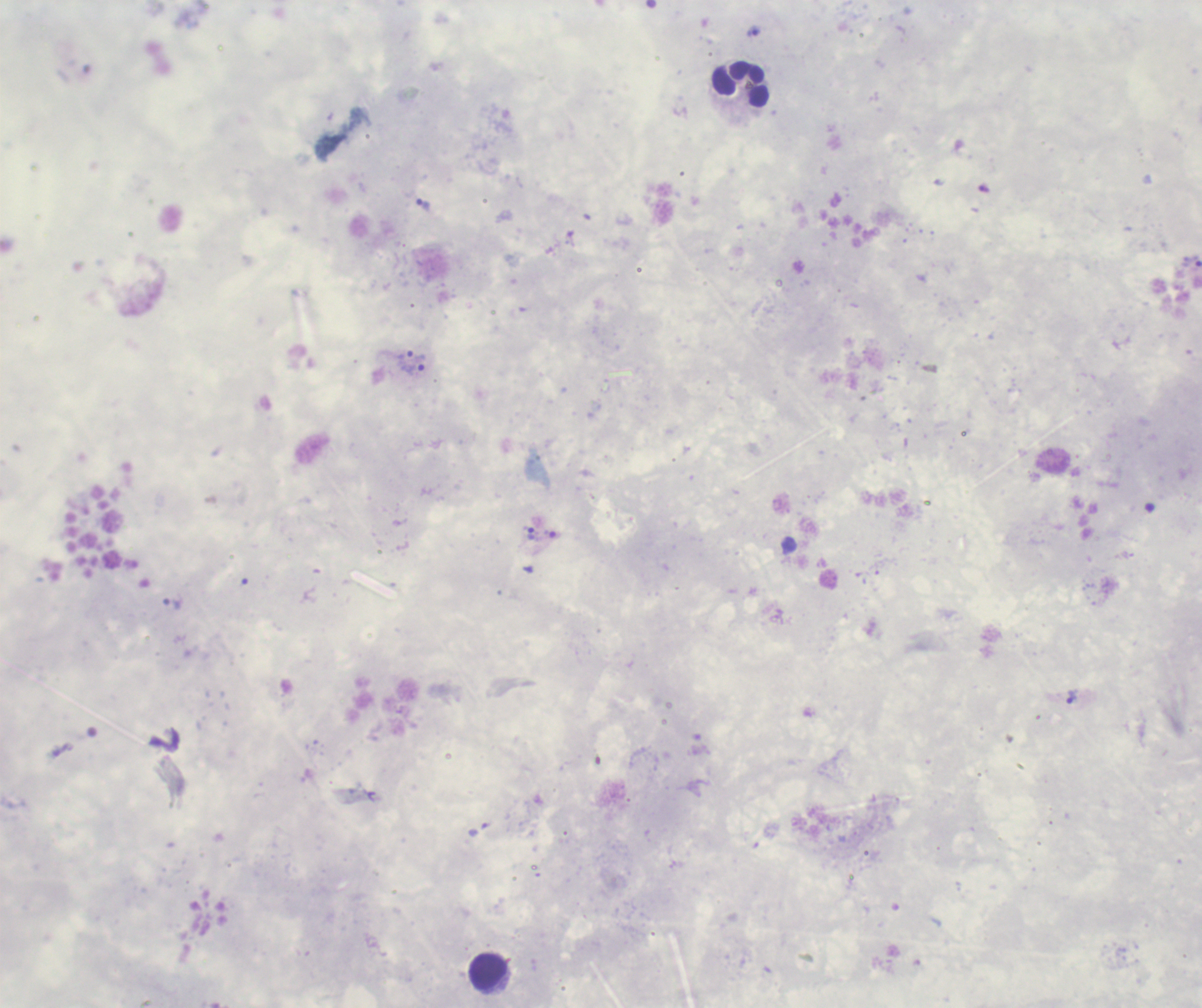 Approximate centers as (x, y) in pixels. Trophozoite locations: (753, 31), (423, 205), (406, 362), (422, 363), (532, 535), (173, 604), (1073, 697). Leukocyte locations: (741, 84), (490, 973). Image is 1202×1008 pixels. Romanowsky-stained preparation. Captured at 100x magnification. Result: Plasmodium parasites detected. Previously used in an actual diagnosis. Background quality: poor. Thick blood smear. Single field of view.